Classify this cell by malaria status.
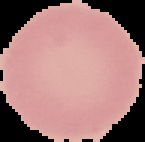
Uninfected.

Summary:
  - Image size: 145×142 pixels
  - Preparation: thin blood smear
  - Image type: segmented cell region on a black background